Name the blood parasite species.
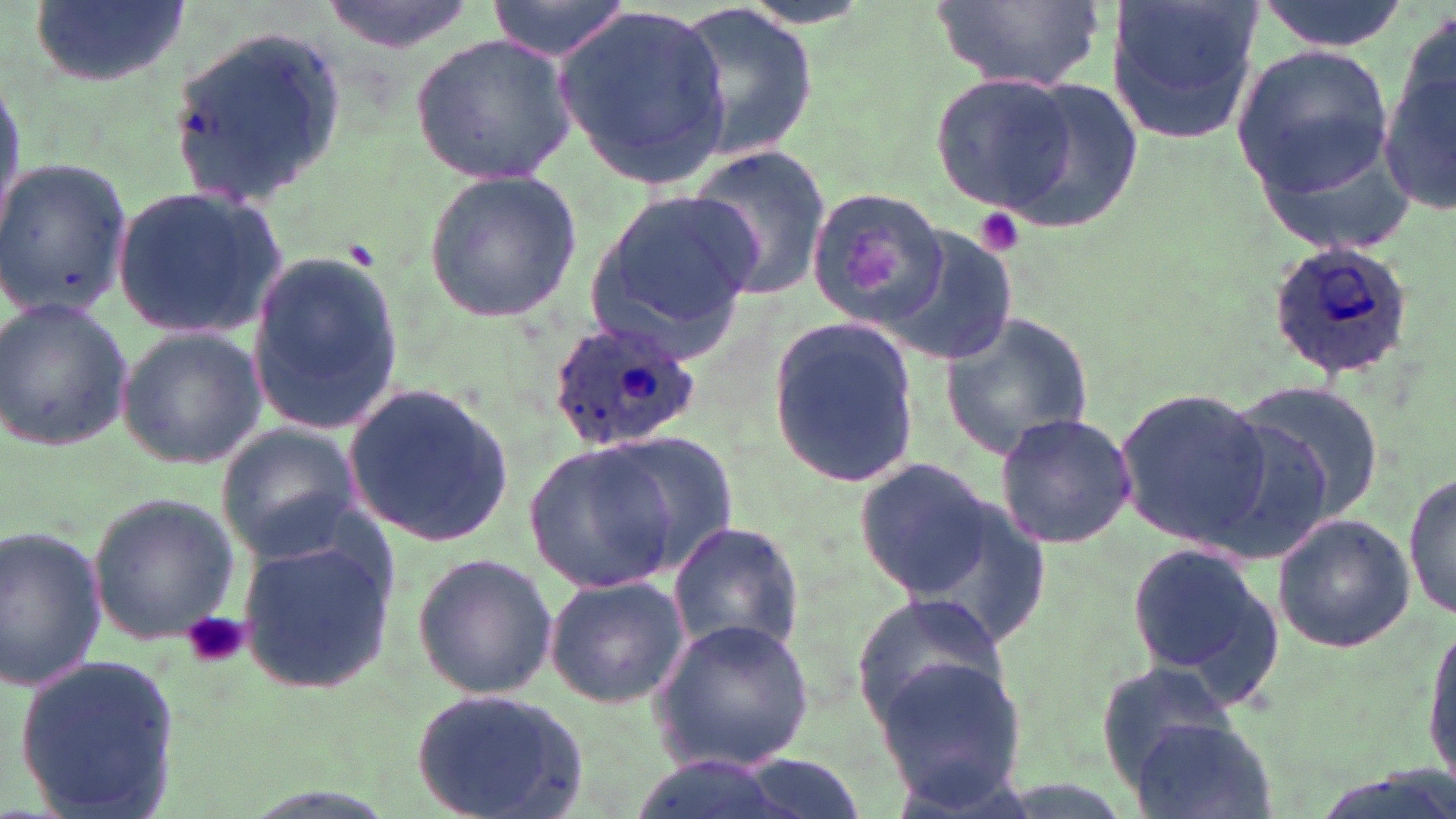

Plasmodium ovale.

platelet locations = approximate bounding boxes as named x1/y1/x2/y2 corners in pixels: (x1=970, y1=208, x2=1027, y2=258), (x1=181, y1=610, x2=249, y2=671)
stain = May-Grünwald-Giemsa
magnification = 1000x
field of view = one of a larger specimen
uninfected red blood cell locations = approximate bounding boxes as named x1/y1/x2/y2 corners in pixels: (x1=28, y1=0, x2=192, y2=90), (x1=315, y1=0, x2=482, y2=56), (x1=481, y1=0, x2=633, y2=60), (x1=929, y1=0, x2=1105, y2=92), (x1=1249, y1=0, x2=1411, y2=52), (x1=675, y1=2, x2=816, y2=169), (x1=1106, y1=2, x2=1265, y2=143), (x1=554, y1=10, x2=733, y2=185), (x1=1383, y1=10, x2=1456, y2=216), (x1=163, y1=28, x2=351, y2=204), (x1=409, y1=31, x2=575, y2=188), (x1=1233, y1=44, x2=1397, y2=196), (x1=0, y1=73, x2=26, y2=230), (x1=928, y1=73, x2=1090, y2=220), (x1=991, y1=74, x2=1142, y2=234), (x1=1255, y1=141, x2=1419, y2=254), (x1=686, y1=146, x2=831, y2=301), (x1=0, y1=158, x2=134, y2=318), (x1=420, y1=168, x2=582, y2=324), (x1=112, y1=184, x2=286, y2=340), (x1=807, y1=185, x2=949, y2=325), (x1=582, y1=194, x2=757, y2=358), (x1=883, y1=228, x2=1019, y2=370), (x1=243, y1=245, x2=405, y2=440), (x1=0, y1=296, x2=134, y2=454), (x1=937, y1=310, x2=1098, y2=461), (x1=767, y1=314, x2=921, y2=488), (x1=118, y1=324, x2=265, y2=470), (x1=1230, y1=379, x2=1389, y2=538), (x1=341, y1=380, x2=517, y2=548), (x1=1112, y1=383, x2=1276, y2=550), (x1=993, y1=413, x2=1139, y2=548), (x1=215, y1=425, x2=362, y2=561), (x1=591, y1=433, x2=738, y2=581), (x1=524, y1=440, x2=685, y2=595), (x1=854, y1=458, x2=999, y2=598), (x1=1405, y1=471, x2=1455, y2=623), (x1=885, y1=476, x2=1058, y2=653), (x1=85, y1=491, x2=239, y2=645), (x1=1272, y1=511, x2=1415, y2=653), (x1=666, y1=521, x2=805, y2=658), (x1=0, y1=526, x2=108, y2=693), (x1=233, y1=528, x2=398, y2=695), (x1=1126, y1=538, x2=1283, y2=701), (x1=411, y1=551, x2=558, y2=700), (x1=542, y1=573, x2=688, y2=710), (x1=851, y1=594, x2=1010, y2=728), (x1=1422, y1=613, x2=1456, y2=790), (x1=651, y1=618, x2=816, y2=772), (x1=16, y1=652, x2=183, y2=817), (x1=871, y1=653, x2=1028, y2=807), (x1=1095, y1=659, x2=1240, y2=780), (x1=410, y1=690, x2=589, y2=816), (x1=1130, y1=718, x2=1276, y2=819)
modality = optical microscopy
Plasmodium ovale-infected red blood cell locations = approximate bounding boxes as named x1/y1/x2/y2 corners in pixels: (x1=1263, y1=240, x2=1413, y2=382), (x1=548, y1=315, x2=704, y2=453)
image size = 1456×819 pixels
preparation = thin blood smear